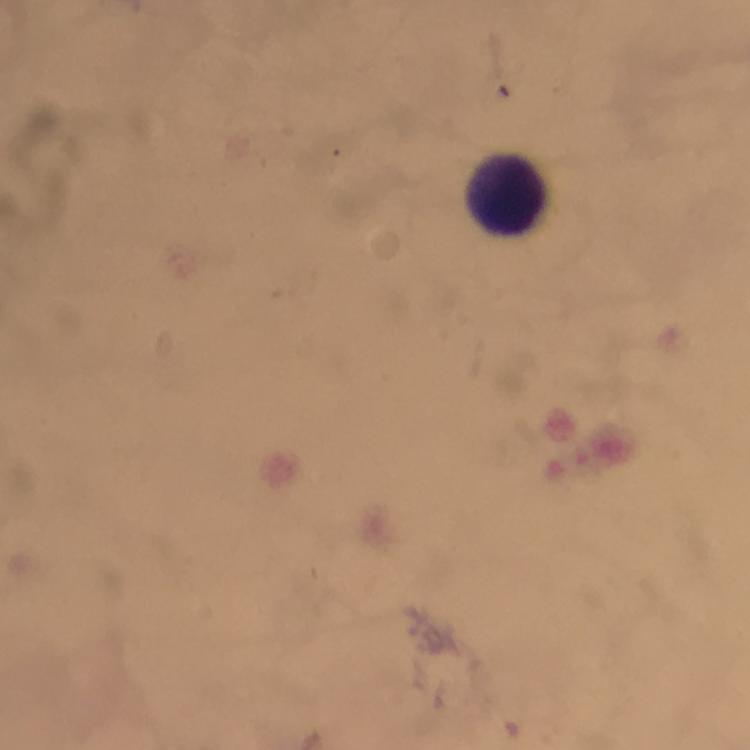
Approximate centers as {x, y} in pixels. Leukocyte locations: {504, 193}. Thick blood film. Image is 750×750 pixels. Immersion oil was used. Giemsa-stained preparation. Photographed with a smartphone mounted on the microscope. From a malaria diagnostic workup. At 100x magnification. A crop from one field of view. Malaria parasites: none seen.